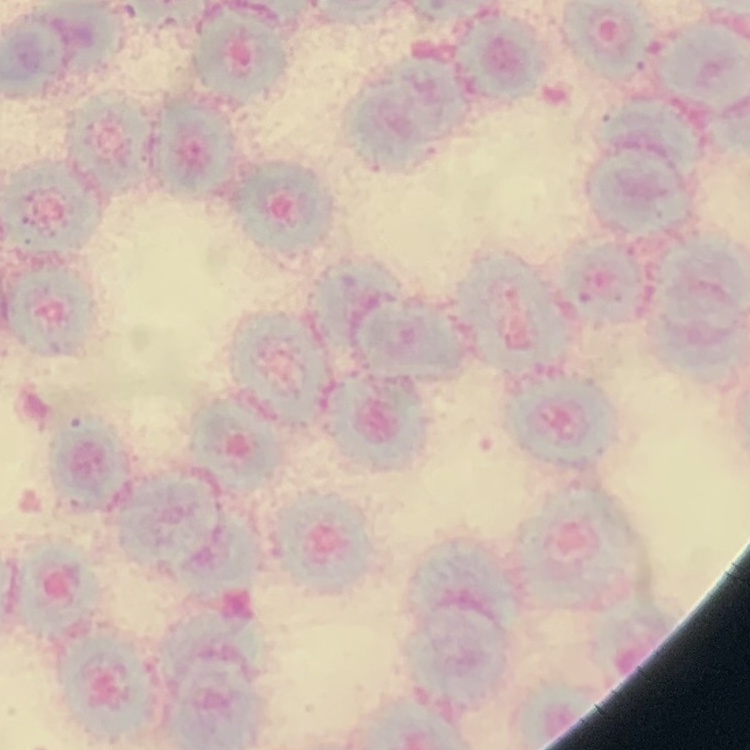

The erythrocytes show rouleaux formation. Thin blood film. One tile cut from a larger photomicrograph. Field's or Giemsa stain.